Give the position of every malaria parasite.
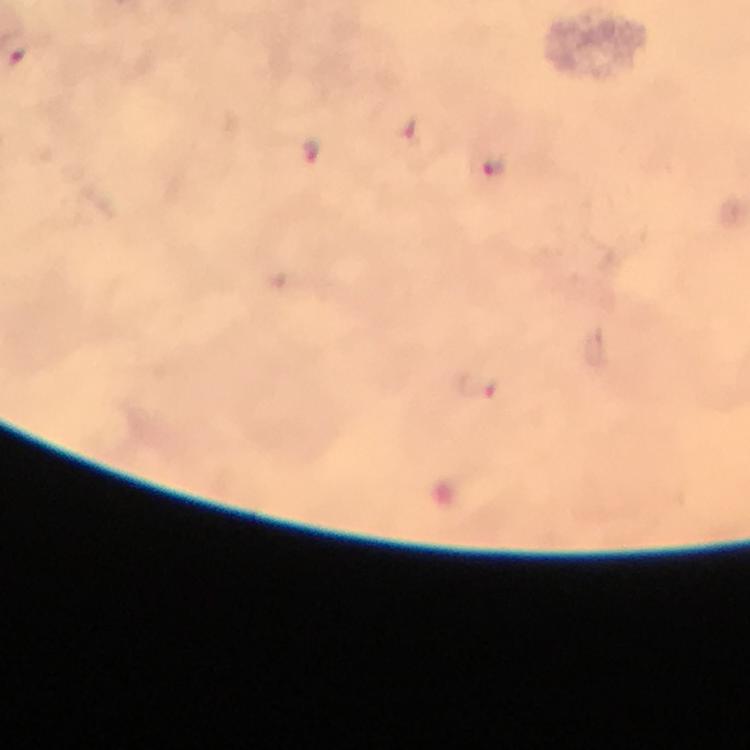

Approximate object centers, in pixels from the top-left corner.
Malaria parasites: (x=410, y=131), (x=311, y=153), (x=494, y=166), (x=477, y=386).

100x magnification. Image is 750×750 pixels. Photographed through the microscope with a smartphone camera. Immersion oil applied. A crop from one field of view. Thick blood film. Giemsa stain. From a diagnostic examination for malaria.